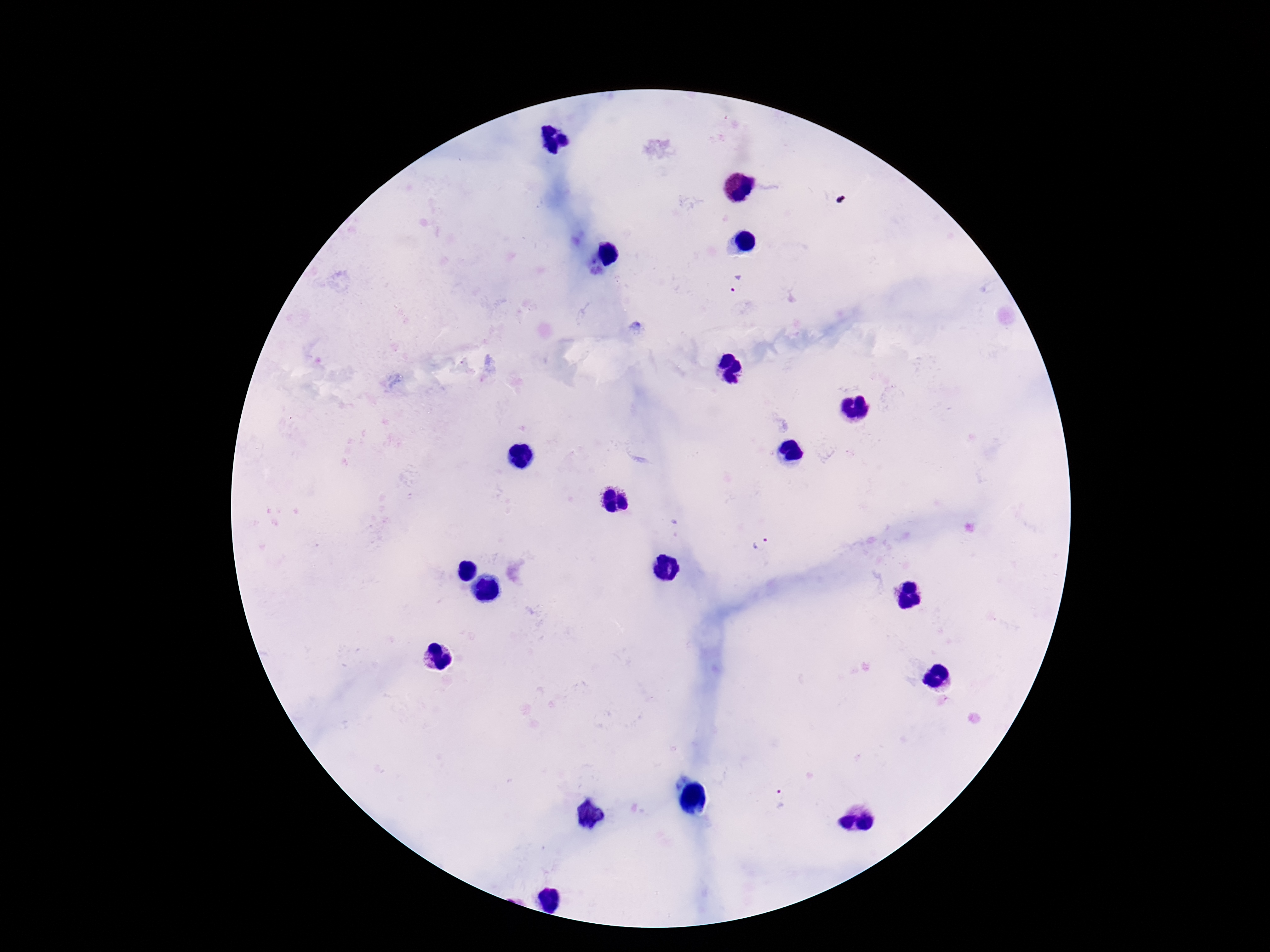 Approximate centers as {x, y} in pixels. Plasmodium parasite locations: {739, 286}, {762, 544}, {783, 800}. Patient malaria status: positive. Thick peripheral-blood smear. Image is 1270×952 pixels. Single field of view. Photographed through the microscope eyepiece with a smartphone camera. 100x magnification. Giemsa-stained preparation.